Name the parasite shown.
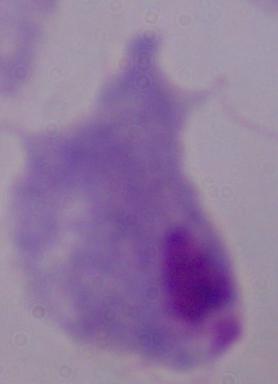
This is a trichomonad.

Summary:
  - Magnification: 1000x
  - Modality: photomicrograph